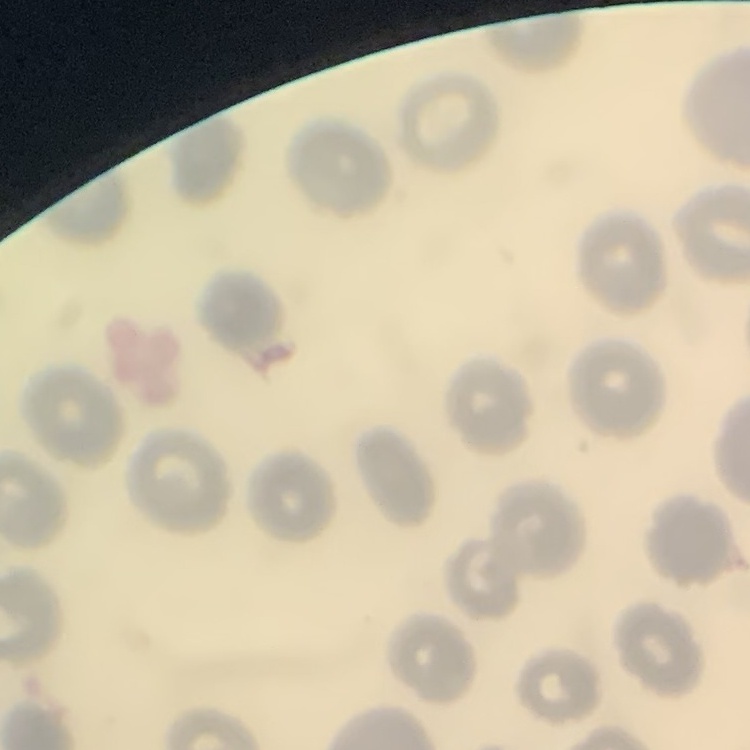
Summary:
  - Red blood cell morphology: no rouleaux formation
  - Stain: Field's or Giemsa
  - Preparation: thin blood smear
  - Image type: square crop of a larger photomicrograph